State which parasite is depicted.
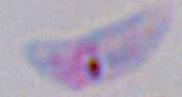
Toxoplasma gondii.

1000x magnification. Photomicrograph.